Classify this cell by malaria status.
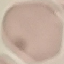

Uninfected.

preparation = thin smear
stain = Giemsa
image type = cell patch, automatically extracted from a larger field of view and resized to 64 × 64 pixels
capture = smartphone through the microscope eyepiece